Report the malaria status of this cell.
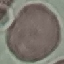

Uninfected.

Thin blood smear. Automatically extracted cell patch, resized to 64 × 64 pixels. Giemsa-stained preparation. Acquired by smartphone through the microscope eyepiece.